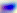

Summary:
  - Modality: photomicrograph
  - Identification: Toxoplasma gondii
  - Magnification: 400x